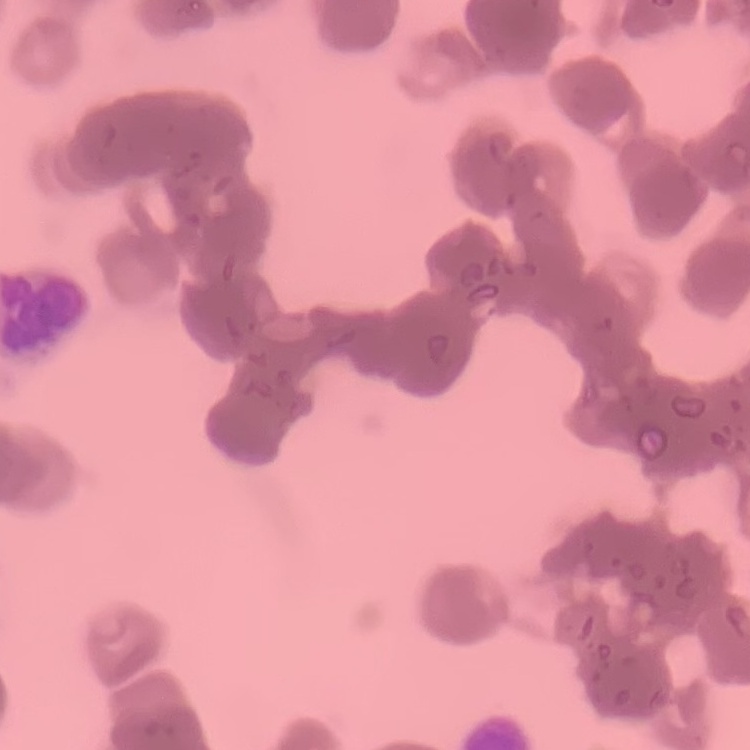 The erythrocytes exhibit rouleaux formation. Stained with either Field's or Giemsa. Thin blood film. One tile cut from a larger photomicrograph.